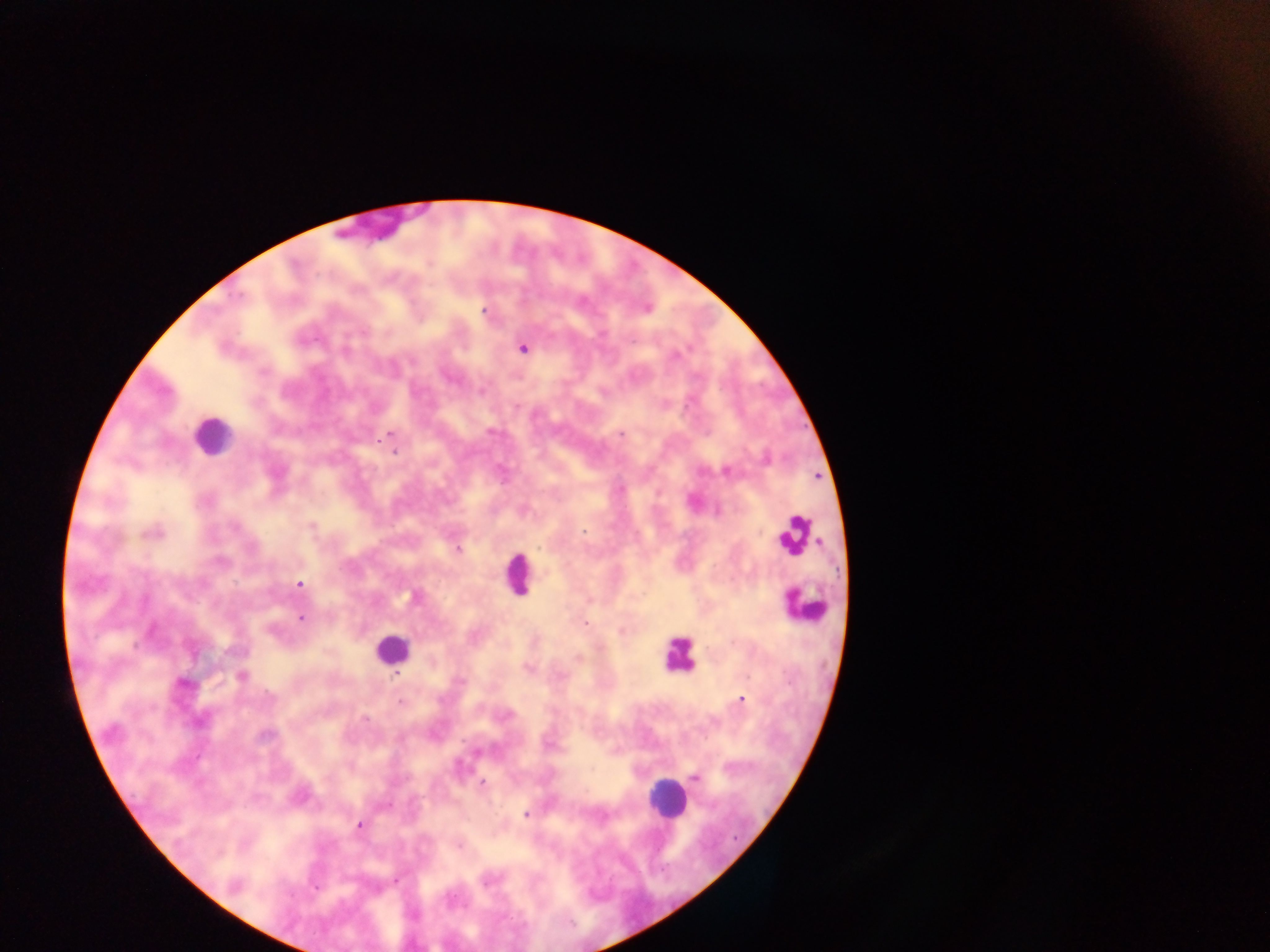

{
  "capture": "mobile-phone photograph through a microscope",
  "preparation": "thick blood film",
  "field_of_view": "single",
  "plasmodium_parasite_locations": "approximate centers as [x, y] in pixels: [427, 265], [239, 294], [581, 301], [483, 312], [600, 333], [303, 338], [348, 342], [522, 350], [450, 376], [481, 389], [602, 391], [663, 405], [516, 408], [390, 432], [490, 432], [622, 434], [378, 437], [395, 451], [725, 470], [700, 473], [818, 477], [693, 502], [718, 509], [311, 529], [582, 530], [459, 549], [298, 582], [408, 597], [300, 616], [584, 622], [271, 629], [622, 629], [579, 657], [528, 668], [397, 674], [241, 677], [183, 682], [742, 700], [400, 701], [504, 713], [365, 716], [473, 752], [694, 778], [480, 781], [527, 814], [358, 825], [458, 845], [487, 879]",
  "leukocyte_locations": "approximate centers as [x, y] in pixels: [213, 440], [794, 533], [517, 579], [804, 602], [397, 647], [679, 660], [668, 797]",
  "image_size": "1270×952 pixels",
  "country": "Ghana"
}